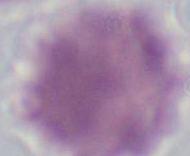 1000x magnification. Photomicrograph. A red blood cell is shown.